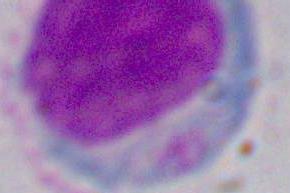
1000x magnification. Photomicrograph. A white blood cell is shown.